State which parasite is depicted.
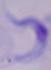

A trypanosome.

Micrograph. 1000x magnification.